Identify the parasite.
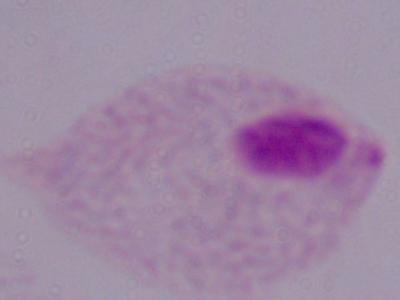
A trichomonad.

Summary:
  - Magnification: 1000x
  - Modality: micrograph